Outline each blood parasite and name the species.
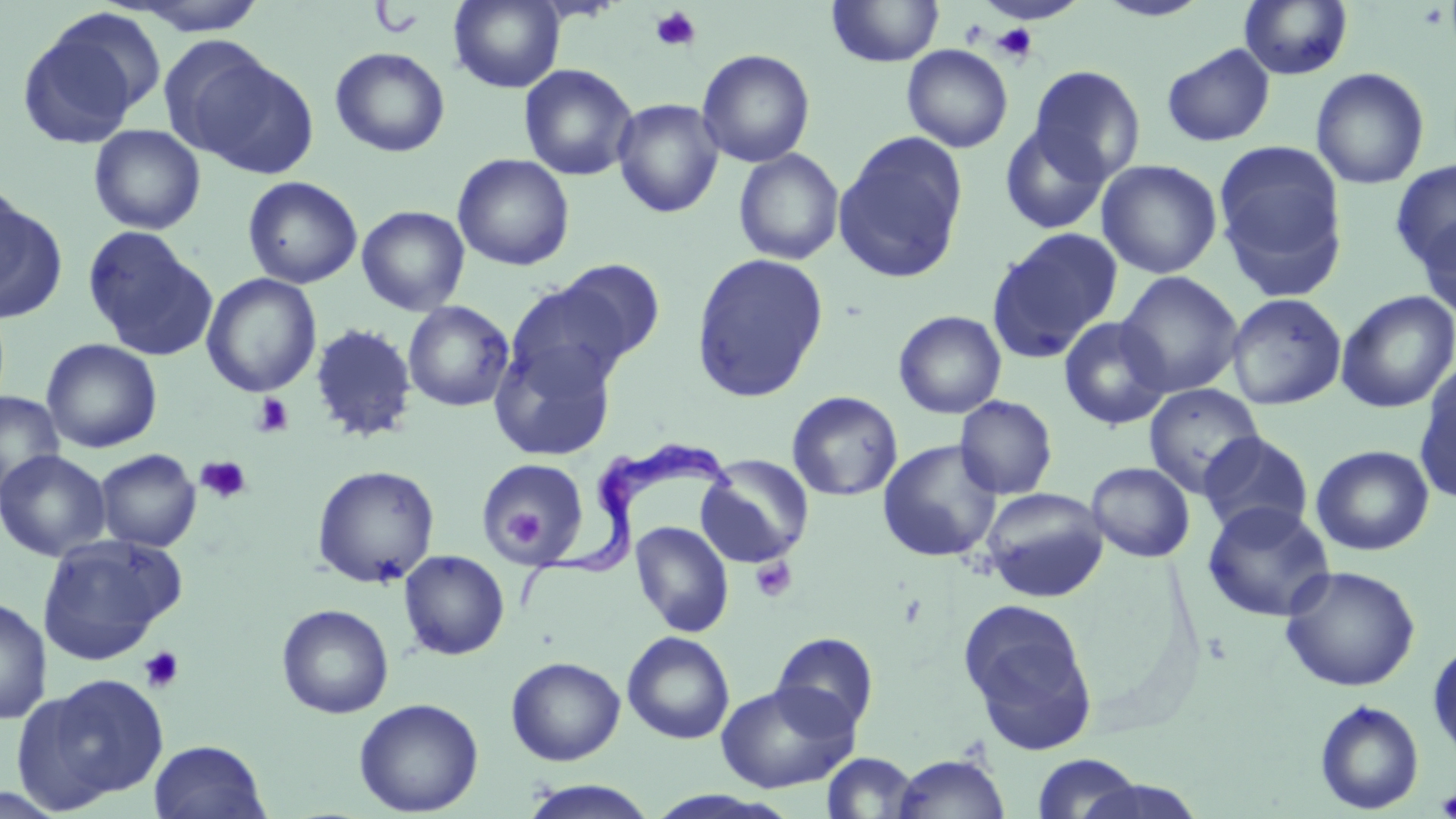

Approximate bounding boxes as [x1, y1, x2, y2] in pixels.
Trypanosoma brucei: [519, 440, 734, 617].
No Plasmodium falciparum, Plasmodium ovale, Plasmodium malariae, Plasmodium vivax, or Babesia divergens observed.

{
  "slide_level_diagnosis": "Trypanosoma brucei",
  "modality": "optical microscopy",
  "uninfected_red_blood_cell_locations": "approximate bounding boxes as [x1, y1, x2, y2] in pixels: [448, 0, 565, 93], [826, 0, 945, 67], [1094, 0, 1212, 22], [114, 1, 271, 36], [979, 1, 1089, 26], [1239, 1, 1353, 80], [16, 13, 157, 150], [1161, 43, 1275, 147], [902, 44, 1013, 153], [330, 47, 450, 158], [174, 48, 317, 178], [697, 49, 815, 168], [518, 63, 638, 181], [1029, 65, 1146, 183], [1310, 67, 1430, 190], [611, 98, 724, 218], [999, 123, 1111, 235], [88, 124, 206, 234], [833, 131, 969, 284], [1212, 139, 1349, 298], [733, 148, 845, 266], [452, 153, 575, 271], [1096, 159, 1222, 279], [1389, 159, 1456, 273], [242, 176, 363, 289], [0, 186, 65, 324], [356, 205, 470, 316], [1415, 213, 1456, 322], [81, 226, 216, 360], [985, 227, 1123, 363], [691, 253, 829, 403], [552, 259, 666, 366], [1116, 271, 1243, 398], [202, 273, 322, 398], [504, 278, 635, 401], [1336, 291, 1456, 413], [1226, 293, 1347, 410], [403, 300, 514, 412], [893, 310, 1007, 419], [1058, 316, 1172, 431], [309, 323, 419, 443], [489, 333, 620, 463], [41, 338, 163, 454], [1414, 364, 1456, 506], [1144, 383, 1265, 498], [787, 390, 903, 501], [0, 391, 64, 501], [954, 395, 1058, 500], [1197, 431, 1314, 538], [878, 440, 1002, 562], [1310, 445, 1434, 556], [94, 448, 201, 552], [0, 449, 110, 561], [696, 455, 814, 568], [477, 459, 587, 566], [1086, 461, 1195, 562], [312, 464, 440, 588], [980, 487, 1109, 602], [1201, 500, 1336, 623], [630, 520, 734, 637], [36, 534, 184, 664], [398, 550, 510, 660], [1279, 564, 1421, 692], [0, 595, 52, 726], [957, 598, 1099, 753], [276, 603, 394, 719], [622, 631, 735, 745], [770, 632, 880, 736], [1427, 639, 1456, 762], [505, 656, 626, 765], [20, 674, 171, 810], [715, 681, 859, 794], [353, 698, 484, 816], [1314, 699, 1424, 814], [148, 740, 270, 819], [821, 752, 921, 817], [891, 753, 1009, 818], [1030, 753, 1145, 819], [1072, 778, 1209, 819], [518, 780, 658, 818]",
  "stain": "May-Grünwald-Giemsa",
  "preparation": "thin blood film",
  "image_size": "1456×819 pixels",
  "field_of_view": "one of a larger specimen",
  "platelet_locations": "approximate bounding boxes as [x1, y1, x2, y2] in pixels: [649, 5, 702, 52], [992, 23, 1038, 64], [252, 392, 294, 438], [195, 455, 251, 503], [500, 509, 549, 546], [750, 556, 797, 603], [138, 646, 184, 694], [1435, 788, 1456, 817]",
  "magnification": "1000x"
}